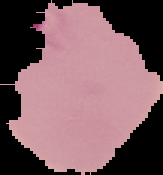
Cell region segmented out of the field of view; the surrounding area is masked to black. From a thin blood smear. Result: malaria parasites identified. Image is 163×175 pixels.